Report the malaria status of this cell.
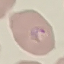
Parasitized.

capture = smartphone through the microscope eyepiece
image type = cell patch, automatically extracted from a larger field of view and resized to 64 × 64 pixels
preparation = thin blood smear
stain = Giemsa